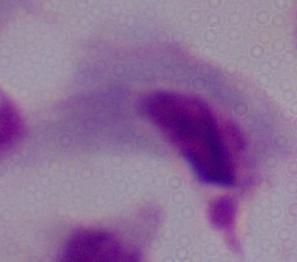
Captured at 1000x magnification. Photomicrograph. A trichomonad is shown.